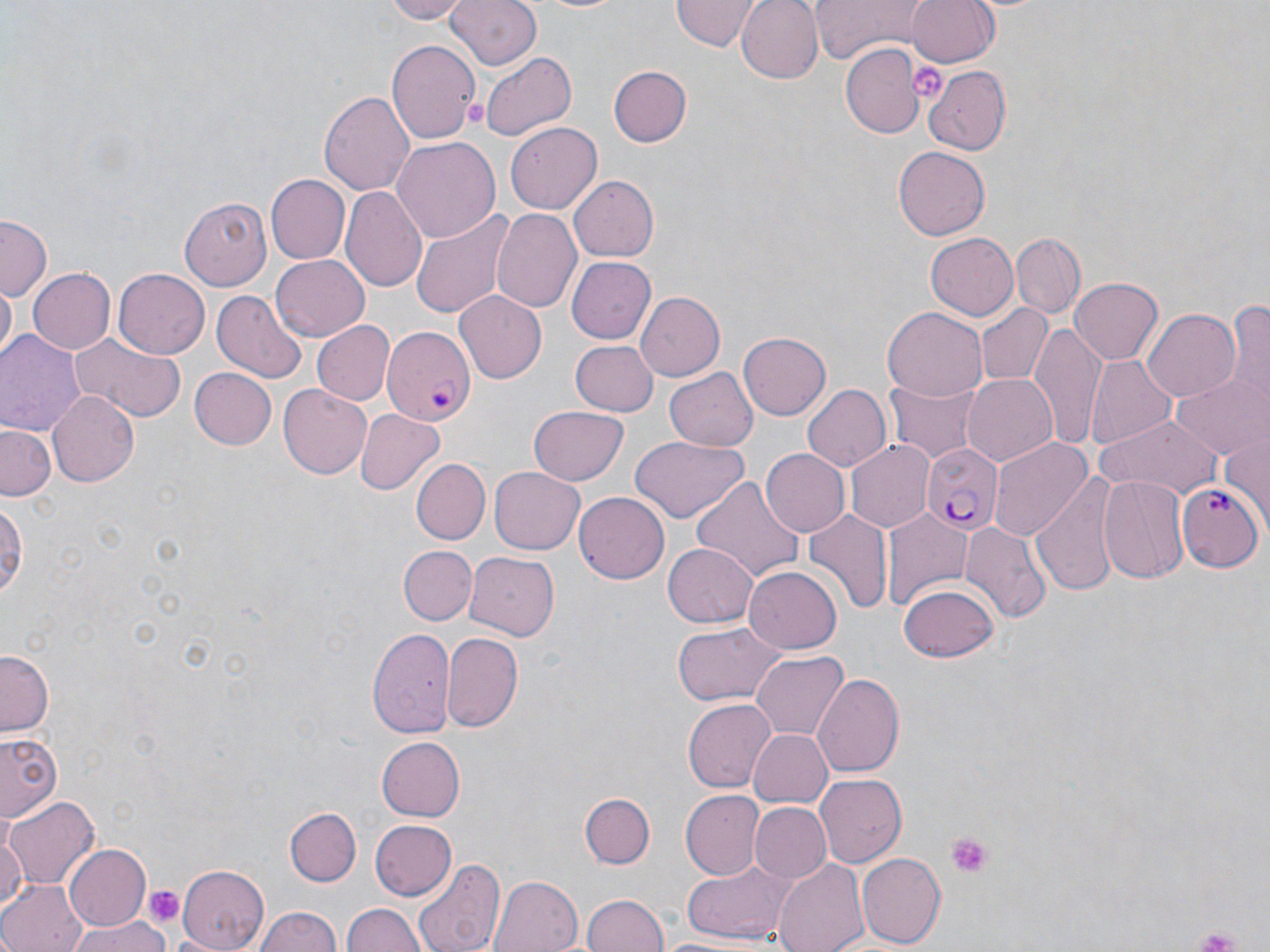

Approximate bounding boxes as (x1, y1, x2, y2) in pixels. Plasmodium falciparum-infected red blood cell locations: (380, 328, 477, 424), (921, 443, 1000, 534), (1178, 482, 1261, 569). Platelet locations: (906, 58, 948, 102), (945, 831, 995, 880), (142, 885, 186, 928). Uninfected red blood cell locations: (380, 0, 470, 23), (446, 0, 542, 72), (672, 0, 760, 51), (738, 0, 822, 83), (904, 0, 1002, 67), (527, 1, 634, 16), (809, 2, 925, 63), (388, 39, 480, 146), (838, 43, 925, 140), (481, 51, 577, 141), (607, 66, 690, 147), (922, 67, 1013, 154), (318, 90, 416, 196), (504, 122, 604, 214), (390, 136, 499, 244), (894, 146, 991, 241), (265, 175, 350, 265), (567, 175, 658, 261), (343, 186, 426, 292), (181, 195, 275, 290), (411, 206, 517, 318), (490, 209, 584, 315), (0, 217, 52, 301), (1011, 232, 1083, 317), (926, 234, 1018, 319), (269, 256, 370, 340), (566, 257, 655, 344), (25, 268, 116, 355), (113, 268, 210, 359), (1071, 277, 1162, 364), (2, 282, 17, 360), (209, 289, 308, 383), (454, 292, 546, 384), (637, 292, 725, 380), (1224, 295, 1270, 414), (973, 303, 1054, 387), (883, 306, 988, 402), (1142, 306, 1242, 403), (312, 320, 395, 405), (1030, 323, 1107, 447), (1, 327, 88, 438), (68, 329, 187, 423), (739, 331, 832, 421), (568, 340, 657, 417), (1087, 356, 1180, 449), (187, 367, 276, 450), (662, 367, 755, 451), (1173, 371, 1267, 458), (960, 374, 1058, 467), (888, 376, 982, 462), (803, 383, 892, 472), (278, 384, 371, 479), (47, 390, 142, 487), (529, 406, 630, 485), (354, 408, 445, 498), (1095, 416, 1226, 500), (1, 425, 58, 500), (1219, 431, 1270, 528), (630, 435, 750, 524), (986, 436, 1092, 544), (846, 440, 936, 532), (759, 449, 848, 537), (410, 458, 490, 545), (489, 466, 584, 554), (1031, 470, 1120, 599), (1098, 472, 1191, 584), (694, 475, 804, 586), (574, 492, 671, 584), (0, 496, 27, 604), (804, 510, 892, 618), (882, 511, 973, 611), (962, 521, 1050, 624), (662, 543, 758, 628), (397, 544, 476, 623), (465, 551, 560, 642), (743, 565, 842, 654), (900, 583, 999, 662), (670, 620, 781, 707), (367, 627, 454, 739), (441, 633, 523, 731), (751, 651, 848, 740), (0, 652, 52, 737), (811, 674, 907, 779), (683, 699, 776, 792), (747, 729, 832, 809), (0, 731, 64, 823), (375, 736, 464, 822), (816, 774, 907, 867), (679, 790, 764, 881), (580, 793, 653, 867), (5, 795, 98, 890), (750, 802, 831, 884), (287, 807, 360, 885), (369, 820, 455, 903), (0, 827, 25, 915), (62, 844, 150, 933), (856, 852, 945, 948), (411, 857, 505, 952), (678, 858, 794, 942), (773, 858, 869, 952), (175, 862, 271, 949), (490, 875, 581, 952), (0, 879, 85, 952), (581, 892, 668, 952), (343, 901, 426, 952), (251, 906, 344, 952), (68, 916, 171, 952), (653, 934, 762, 952). Slide-level diagnosis: Plasmodium falciparum. Thin blood smear. Single field of view. May-Grünwald-Giemsa-stained preparation. Light microscopy. 1000x magnification. Image is 1270×952 pixels.